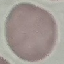
result = negative for malaria parasites
image type = automatically extracted cell patch, resized to 64 × 64 pixels
stain = Giemsa
capture = smartphone camera at the microscope eyepiece
preparation = thin smear